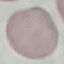

malaria status = uninfected
capture = smartphone through the microscope eyepiece
image type = automatically extracted cell patch, resized to 64 × 64 pixels
preparation = thin blood smear
stain = Giemsa